Classify this cell by malaria status.
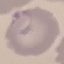
It is parasitized.

Giemsa stain. Acquired by smartphone through the microscope eyepiece. Cell patch, automatically extracted from a larger field of view and resized to 64 × 64 pixels. Thin blood smear.